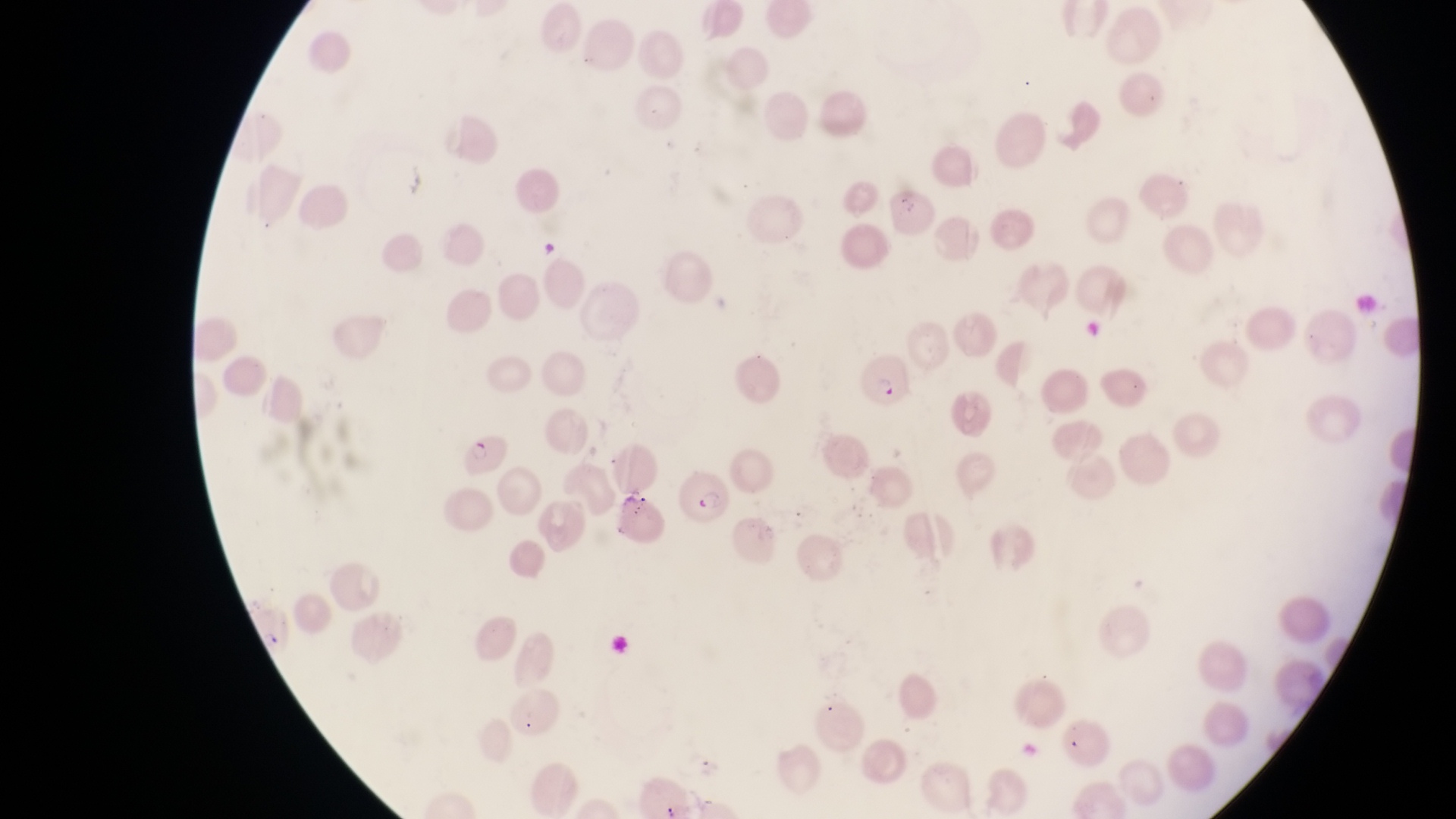
Approximate bounding boxes as left top right bottom in pixels. Parasitised red blood cell locations: 682 472 728 527. Objects each labeled both parasitised red blood cell and gametocyte by the source: 856 359 908 412; 459 431 508 478. Artifact (platelet-like body, stain precipitate, or debris) locations: 532 238 564 268. Thin blood smear. Collected in Uganda. Captured by a smartphone held over the eyepiece of an Olympus CX-23 microscope. Single field of view. Image is 1456×819 pixels. Magnification of 1000x.